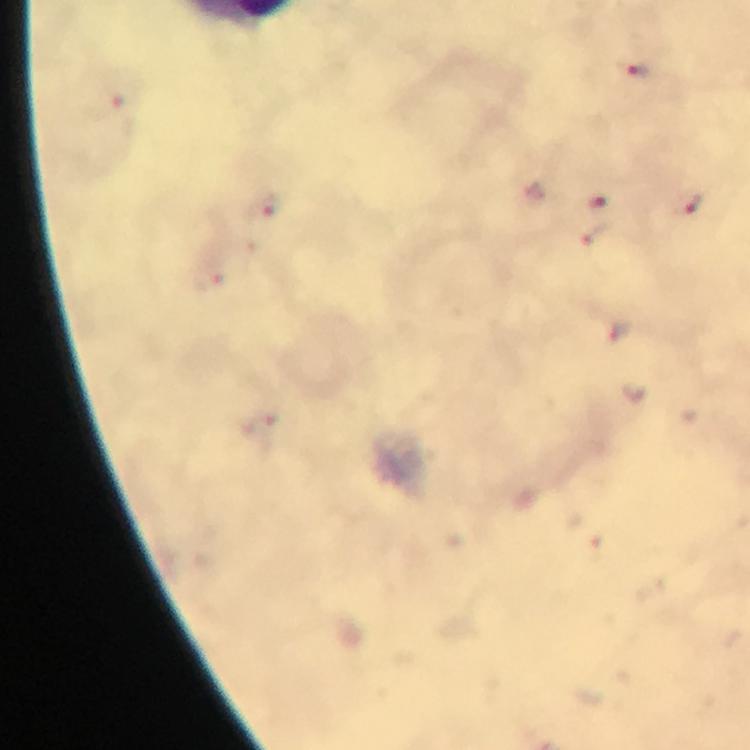
Approximate centers as [x, y] in pixels.
Summary:
  - Malaria parasite locations: [639, 72], [106, 106], [596, 200], [263, 204], [692, 205], [595, 235], [206, 281]
  - Cropped from: a single field of view
  - Image size: 750×750 pixels
  - Stain: Giemsa
  - Preparation: thick blood smear
  - Magnification: 100x
  - Capture: smartphone photograph through a microscope
  - Immersion oil: used
  - Context: from a diagnostic examination for malaria